Give the extent of all Plasmodium vivax-infected red blood cells.
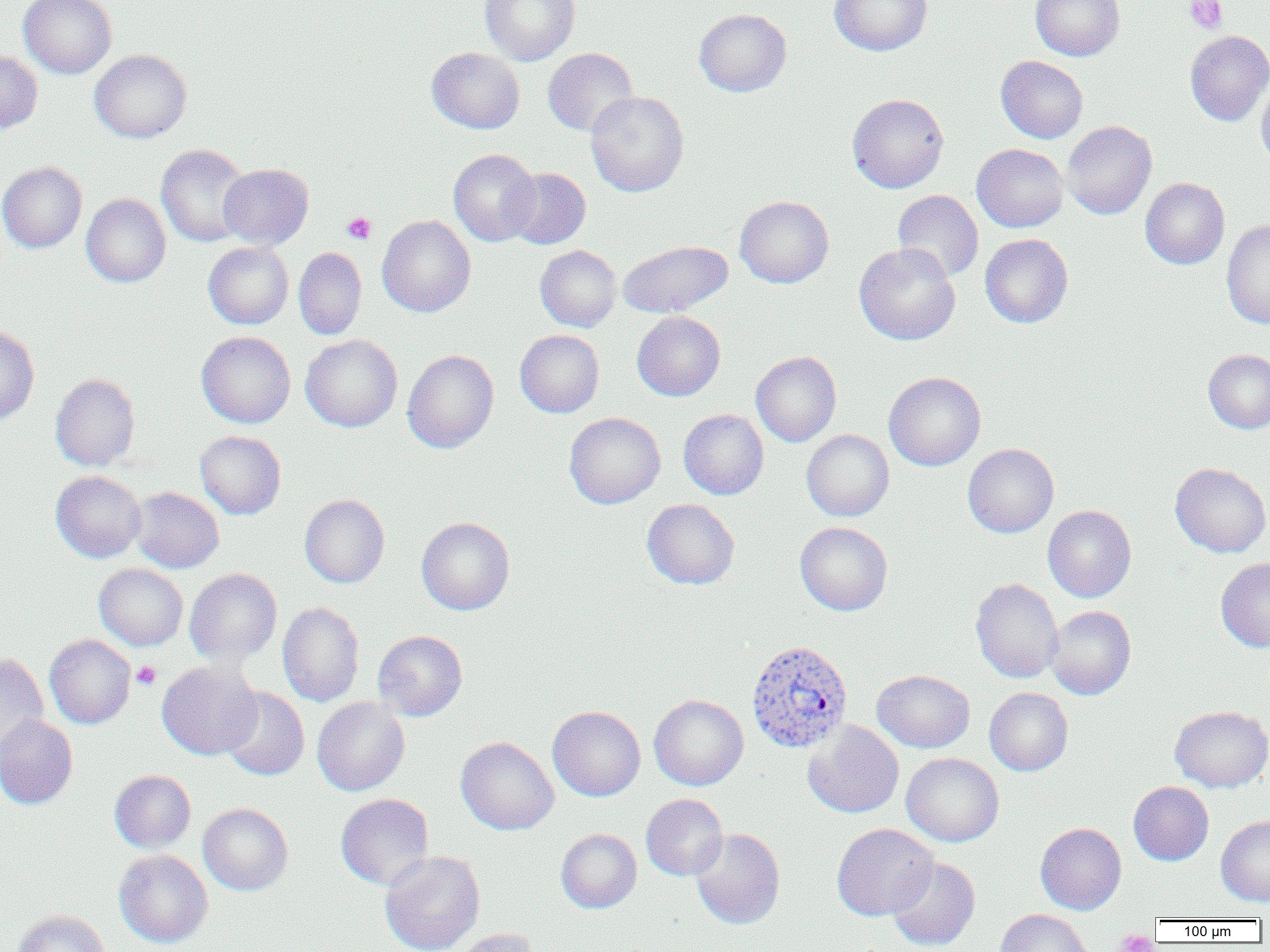
Approximate bounding boxes as (x1,y1)-(x2,y2) corner pairs in pixels.
Plasmodium vivax-infected red blood cells: (746,639)-(853,752).

Platelet locations: (1185,0)-(1228,34), (342,212)-(376,244), (132,661)-(160,690), (1114,929)-(1157,952). Uninfected red blood cell locations: (19,0)-(117,79), (480,0)-(580,65), (830,0)-(932,56), (1030,0)-(1125,61), (694,8)-(791,97), (1185,31)-(1270,125), (427,47)-(524,134), (542,47)-(637,137), (90,49)-(191,143), (0,50)-(42,133), (996,55)-(1088,143), (1256,76)-(1270,168), (585,91)-(688,197), (847,93)-(948,193), (1062,120)-(1157,219), (972,143)-(1069,232), (156,144)-(252,247), (448,149)-(541,246), (0,162)-(87,253), (219,163)-(313,250), (505,167)-(590,249), (1140,177)-(1229,269), (892,190)-(983,281), (81,194)-(170,287), (735,196)-(834,288), (377,215)-(476,317), (1221,218)-(1270,329), (980,234)-(1073,328), (618,240)-(733,317), (202,242)-(293,329), (854,242)-(960,345), (535,245)-(621,332), (293,247)-(366,340), (632,311)-(725,401), (0,324)-(39,425), (515,330)-(604,418), (196,331)-(295,428), (300,334)-(402,432), (302,347)-(497,441), (1203,349)-(1270,434), (402,350)-(498,453), (751,351)-(842,447), (884,371)-(986,471), (51,373)-(140,470), (678,409)-(769,500), (564,412)-(665,509), (801,430)-(894,521), (195,431)-(286,519), (963,443)-(1059,537), (1170,463)-(1270,558), (51,470)-(146,563), (130,487)-(224,573), (299,494)-(389,588), (642,499)-(739,589), (1043,505)-(1136,602), (416,517)-(515,615), (795,522)-(892,615), (1216,558)-(1270,652), (94,563)-(187,651), (184,568)-(282,666), (970,578)-(1063,683), (277,601)-(364,707), (1045,605)-(1136,700), (373,630)-(467,721), (44,635)-(136,729), (0,652)-(49,764), (156,661)-(261,760), (872,669)-(974,753), (220,687)-(309,781), (984,687)-(1073,776), (649,694)-(748,791), (312,696)-(409,796), (547,705)-(646,802), (1169,705)-(1270,792), (0,714)-(78,809), (803,721)-(904,818), (456,736)-(559,835), (901,752)-(1004,847), (109,770)-(196,852), (1128,781)-(1213,866), (335,793)-(434,890), (641,794)-(728,881), (198,803)-(293,895), (1216,815)-(1270,906), (1035,822)-(1126,915), (832,823)-(938,920), (556,828)-(642,913), (690,828)-(786,930), (114,849)-(213,948), (380,850)-(485,952), (886,856)-(980,951), (12,909)-(110,952), (995,909)-(1094,952), (449,929)-(539,952). Slide-level diagnosis: Plasmodium vivax. Image is 1270×952 pixels. Light microscopy. 1000x magnification. Thin blood smear. One field of a larger specimen.